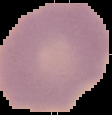

From a thin blood smear. Image is 112×115 pixels. Result: no malaria parasites detected. The area outside the segmented cell region is set to black.